Locate every Plasmodium parasite.
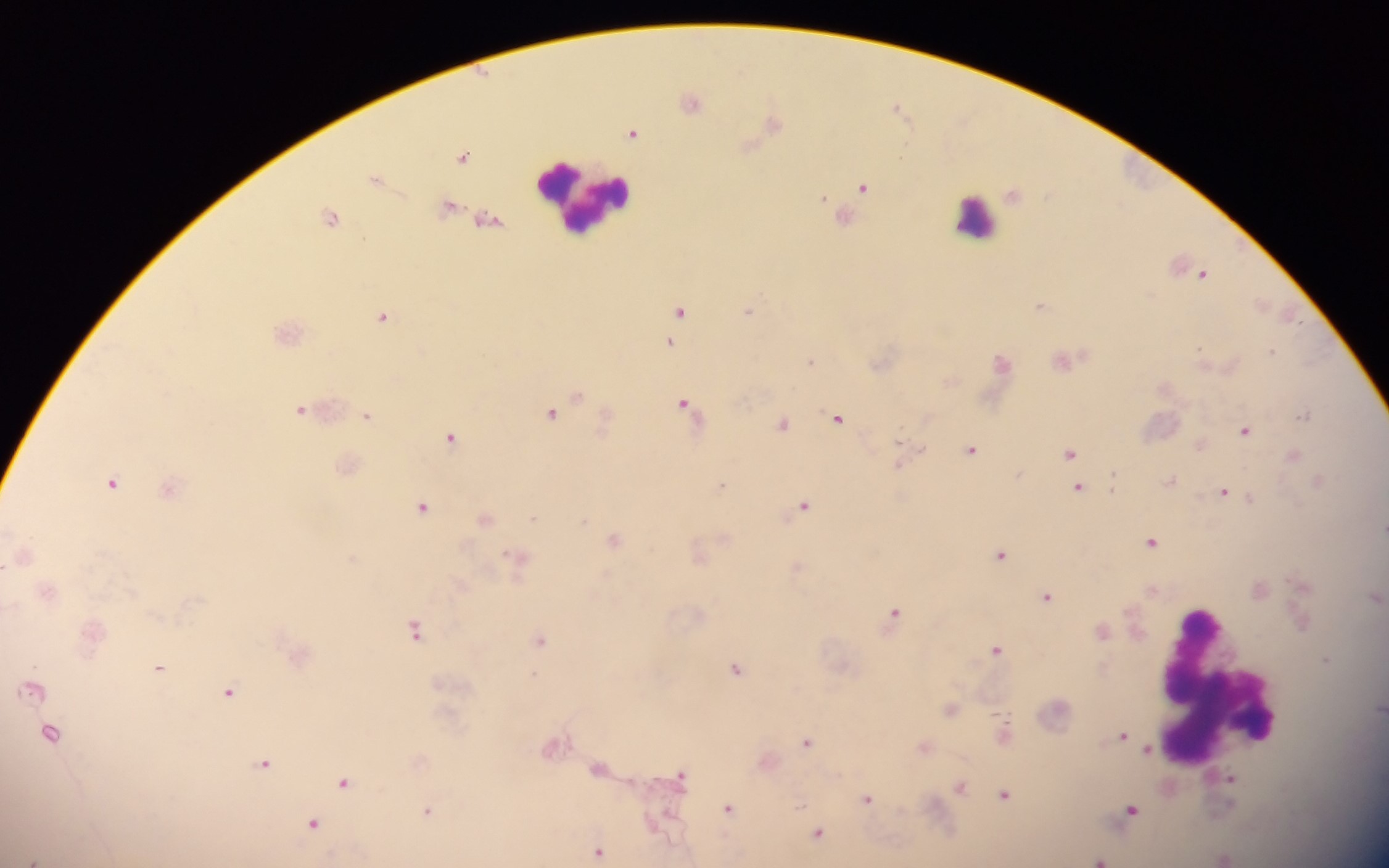

Approximate centers as {x, y} in pixels.
Plasmodium parasites: {692, 101}, {898, 107}, {773, 123}, {632, 133}, {464, 157}, {376, 178}, {863, 186}, {331, 216}, {1204, 274}, {1041, 306}, {679, 309}, {748, 309}, {383, 316}, {1291, 318}, {670, 343}, {1199, 347}, {1272, 350}, {811, 360}, {1064, 360}, {1002, 362}, {685, 403}, {301, 409}, {552, 413}, {367, 415}, {1305, 415}, {837, 417}, {782, 424}, {1245, 430}, {451, 437}, {973, 449}, {1070, 453}, {1293, 456}, {901, 458}, {1171, 480}, {1113, 481}, {1319, 481}, {113, 482}, {721, 486}, {1078, 487}, {1224, 492}, {1251, 500}, {804, 505}, {423, 507}, {485, 518}, {533, 518}, {1383, 528}, {614, 540}, {1152, 542}, {1001, 554}, {5, 566}, {1048, 596}, {895, 612}, {415, 630}, {1103, 630}, {541, 638}, {996, 649}, {1327, 659}, {159, 667}, {737, 668}, {32, 689}, {229, 691}, {951, 709}, {50, 734}, {1123, 735}, {806, 741}, {552, 746}, {924, 747}, {1148, 750}, {264, 763}, {599, 768}, {681, 775}, {1230, 778}, {345, 783}, {961, 786}, {1006, 795}, {867, 798}, {728, 809}, {427, 810}, {1132, 810}, {313, 823}, {818, 833}, {599, 852}, {34, 859}, {1101, 860}.

Leukocyte locations: {586, 196}, {975, 218}, {1217, 684}. Image is 1389×868 pixels. One field of view. Collected in Ghana. Thick blood smear. Mobile-phone photograph taken through the microscope.